Classify this cell by malaria status.
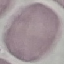

Uninfected.

Summary:
  - Capture: smartphone camera at the microscope eyepiece
  - Image type: cell patch, automatically extracted from a larger field of view and resized to 64 × 64 pixels
  - Preparation: thin smear
  - Stain: Giemsa